Report the malaria status of this cell.
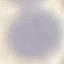

It is uninfected.

stain: Giemsa
capture: smartphone through the microscope eyepiece
image_type: automatically extracted cell patch, resized to 64 × 64 pixels
preparation: thin smear